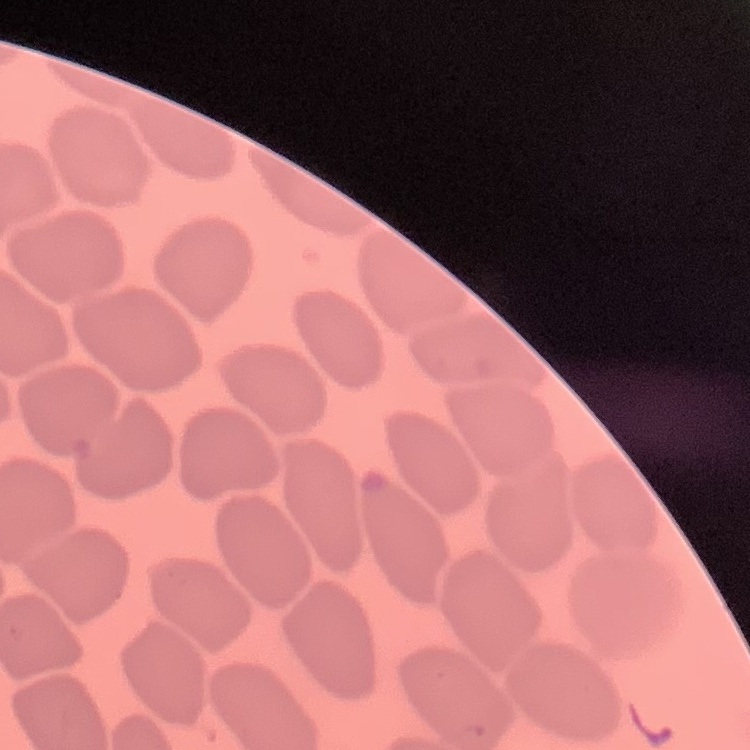
erythrocyte_morphology: no rouleaux formation
stain: Field's or Giemsa
image_type: one tile cut from a larger photomicrograph
preparation: thin peripheral smear